Point out each malaria parasite and each leukocyte.
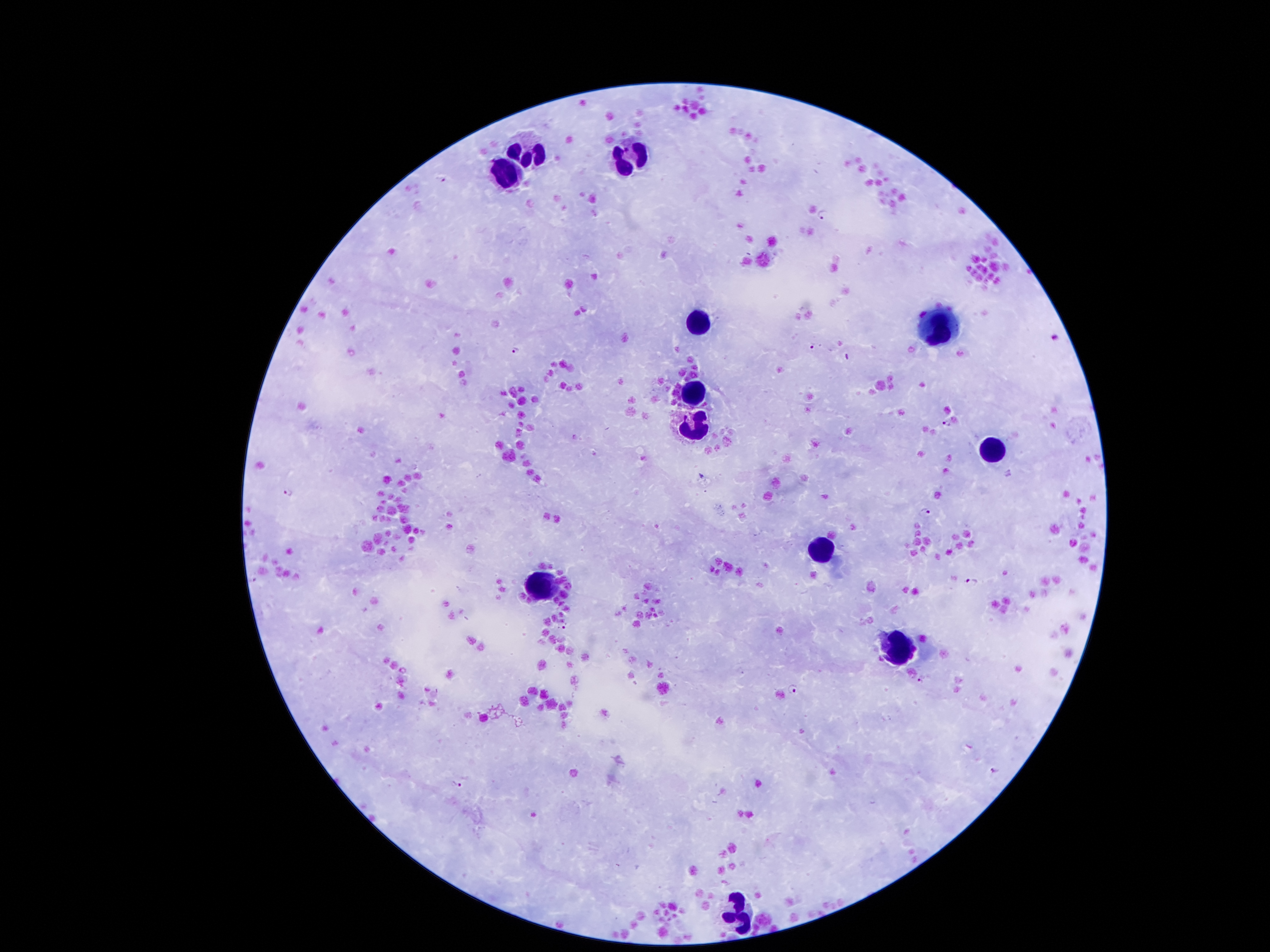

Approximate centers as (x, y) in pixels.
Malaria parasites: (442, 179), (822, 213), (812, 344), (516, 352), (947, 423), (288, 491), (924, 511), (254, 580), (971, 582), (563, 626), (920, 681), (793, 689), (995, 769), (457, 784).
Leukocytes: (529, 155), (631, 156), (502, 171), (696, 327), (938, 328), (694, 394), (694, 428), (987, 452), (821, 549), (539, 583), (888, 644), (737, 918).

preparation = thick blood smear
magnification = 100x
patient malaria status = infected with Plasmodium falciparum
stain = Giemsa
capture = smartphone through the microscope eyepiece
field of view = single
image size = 1270×952 pixels